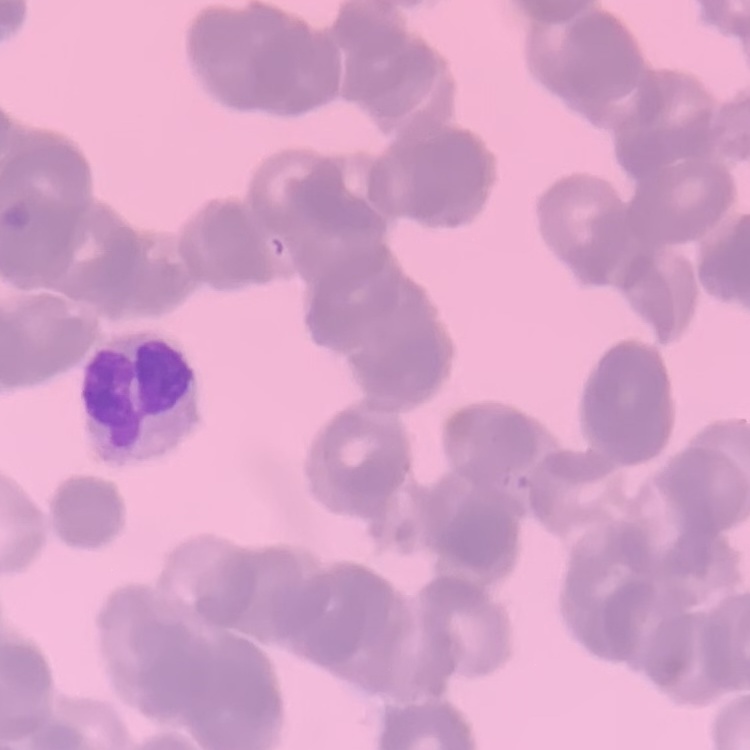 The erythrocytes exhibit rouleaux formation. One tile cut from a larger photomicrograph. Field's or Giemsa stain. Thin blood film.